Name the parasite shown.
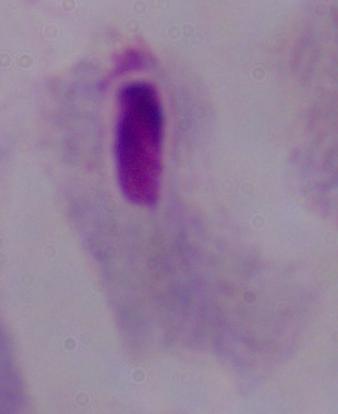
A trichomonad.

modality = photomicrograph
magnification = 1000x